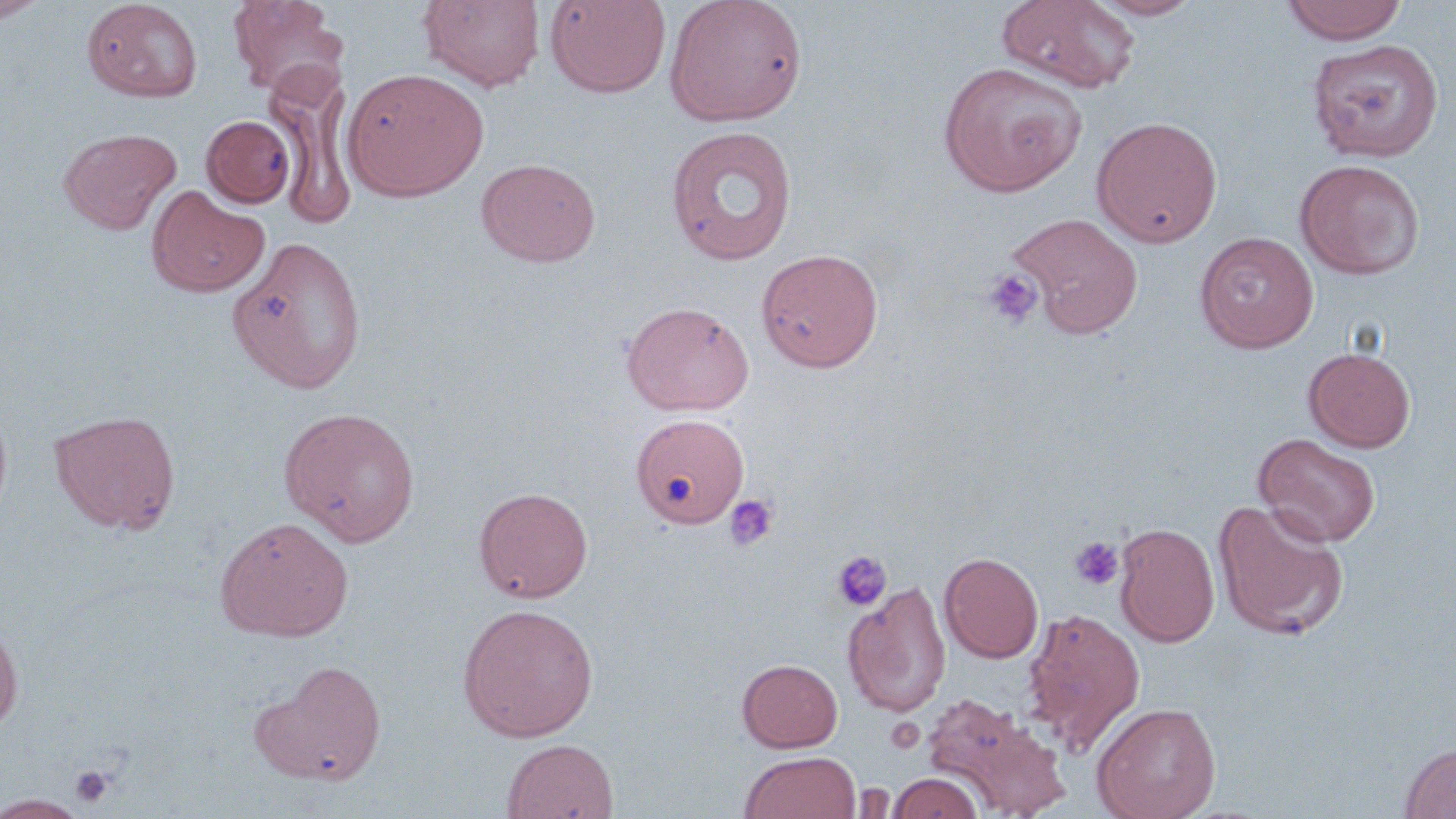
{
  "slide_level_diagnosis": "negative for blood parasites",
  "field_of_view": "single",
  "modality": "light microscopy",
  "platelet_locations": "approximate bounding boxes as (x1,y1)-(x2,y2) corner pairs in pixels: (982,270)-(1042,328), (723,493)-(778,552), (1068,536)-(1125,591), (831,551)-(892,612), (67,764)-(117,809)",
  "magnification": "1000x",
  "preparation": "thin blood film",
  "stain": "May-Grünwald-Giemsa",
  "uninfected_red_blood_cell_locations": "approximate bounding boxes as (x1,y1)-(x2,y2) corner pairs in pixels: (0,0)-(48,23), (82,0)-(202,102), (228,0)-(347,98), (418,0)-(545,92), (545,0)-(671,98), (664,0)-(808,128), (996,0)-(1141,93), (1088,0)-(1206,20), (1281,0)-(1408,44), (1307,39)-(1442,161), (937,61)-(1088,197), (343,67)-(488,202), (271,70)-(360,231), (202,115)-(295,207), (1091,115)-(1223,248), (665,126)-(798,266), (58,127)-(180,235), (477,158)-(600,267), (1295,158)-(1425,279), (147,187)-(267,298), (1006,212)-(1144,339), (1195,231)-(1319,352), (229,236)-(366,395), (756,247)-(884,372), (621,300)-(754,416), (1304,347)-(1416,452), (0,401)-(13,525), (279,407)-(421,545), (49,409)-(181,534), (631,414)-(749,527), (1253,433)-(1381,548), (473,486)-(593,602), (1213,499)-(1348,640), (215,516)-(355,641), (1114,522)-(1220,647), (940,552)-(1043,663), (843,580)-(951,718), (458,603)-(599,742), (1021,607)-(1146,757), (0,622)-(23,733), (737,658)-(843,752), (258,661)-(388,784), (920,694)-(1065,813), (1092,701)-(1221,819), (501,738)-(619,819), (1398,740)-(1456,818), (739,751)-(861,819), (888,773)-(983,819), (1,793)-(91,819)",
  "image_size": "1456×819 pixels"
}